Classify this cell by malaria status.
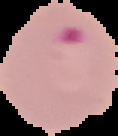
Parasitized.

Summary:
  - Image type: segmented cell region on a black background
  - Image size: 118×136 pixels
  - Preparation: thin blood film